Classify this cell by malaria status.
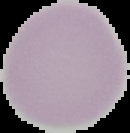

It is uninfected.

From a thin blood film. Segmented cell region on a black background. Image is 130×133 pixels.